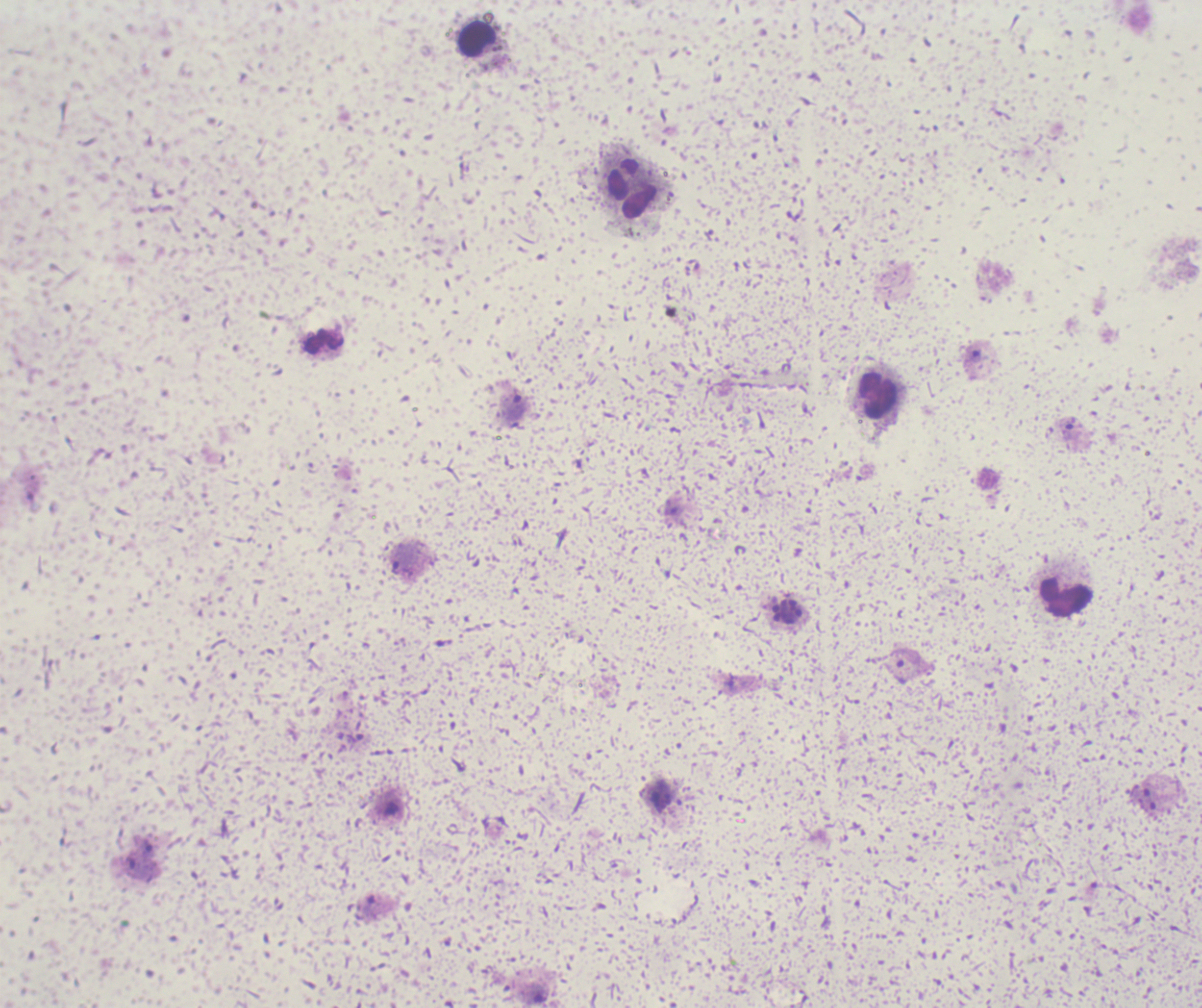
Approximate centers as (x, y) in pixels. Trophozoite locations: (514, 407), (404, 556). Schizont locations: (788, 611). Leukocyte locations: (478, 40), (632, 189), (879, 395), (1066, 599). Life-cycle stages observed: trophozoite, schizont. Image is 1202×1008 pixels. One field from this slide. Background quality: unsatisfactory. Captured at 100x magnification. Romanowsky stain. Previously used in a real diagnosis. Thick blood smear. Result: malaria parasites detected.